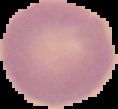
{
  "malaria_status": "uninfected",
  "preparation": "thin blood film",
  "image_size": "118×109 pixels",
  "image_type": "segmented cell region with the area outside set to black"
}